Report the malaria status of this cell.
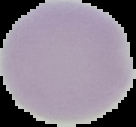

Uninfected.

Cell region segmented out of the field of view; the surrounding area is masked to black. Image is 136×127 pixels. From a thin blood film.